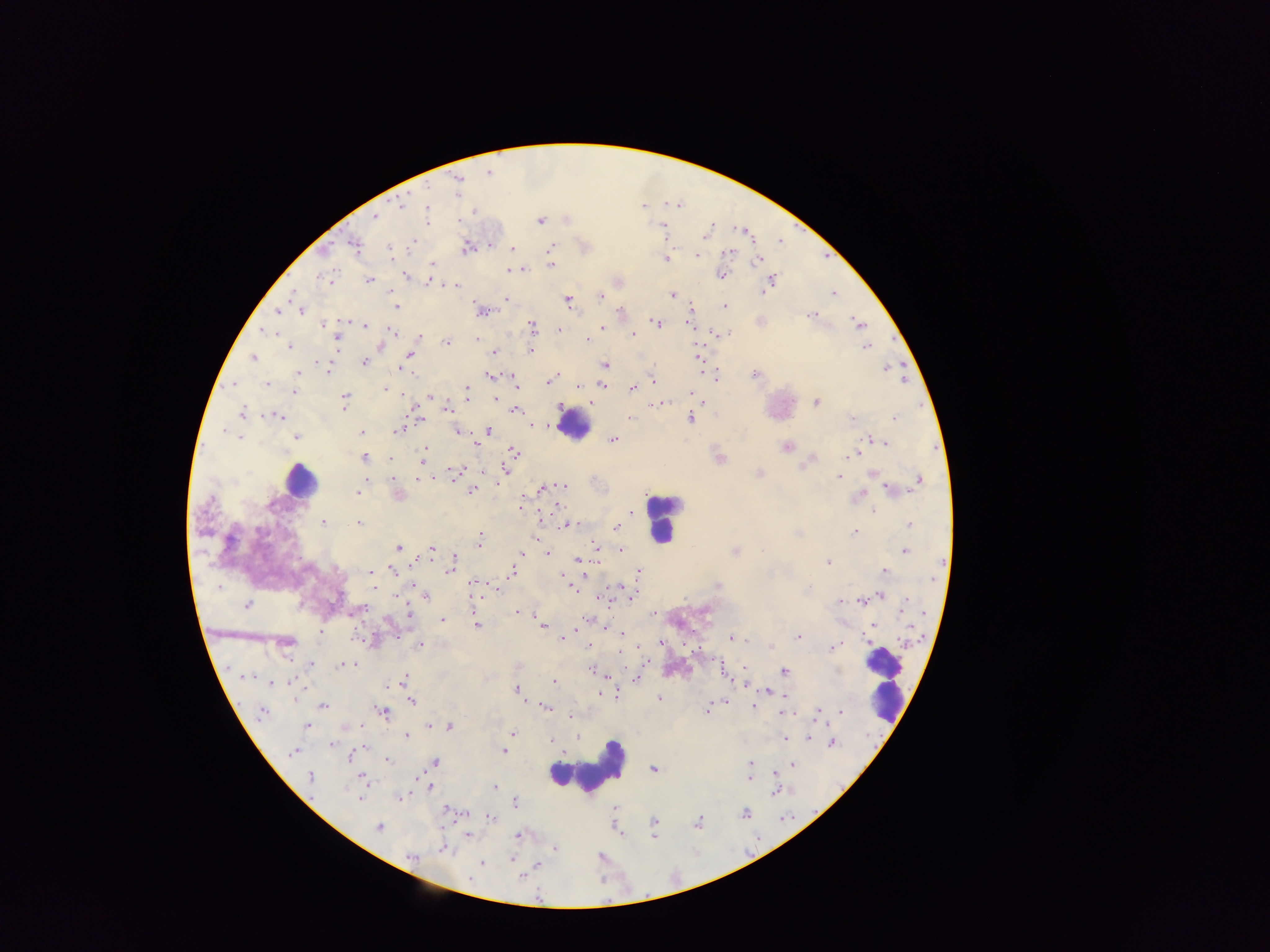
Approximate centers as {x, y} in pixels. Plasmodium parasite locations: {489, 173}, {457, 186}, {402, 205}, {642, 206}, {428, 210}, {375, 215}, {539, 221}, {663, 227}, {742, 230}, {706, 231}, {413, 242}, {355, 246}, {551, 246}, {466, 247}, {389, 249}, {512, 249}, {728, 252}, {697, 255}, {666, 259}, {757, 260}, {432, 264}, {551, 265}, {509, 270}, {516, 270}, {720, 274}, {405, 275}, {327, 277}, {369, 280}, {771, 282}, {454, 285}, {833, 293}, {600, 295}, {672, 295}, {505, 300}, {568, 302}, {396, 306}, {725, 307}, {692, 309}, {277, 310}, {481, 310}, {301, 311}, {621, 311}, {810, 316}, {690, 320}, {656, 323}, {859, 324}, {326, 325}, {365, 325}, {532, 326}, {603, 328}, {559, 330}, {264, 332}, {392, 332}, {633, 334}, {723, 334}, {420, 336}, {337, 338}, {476, 338}, {588, 339}, {446, 342}, {289, 347}, {865, 347}, {532, 350}, {495, 352}, {410, 355}, {253, 358}, {698, 358}, {364, 363}, {604, 365}, {323, 366}, {401, 367}, {885, 368}, {298, 372}, {755, 374}, {490, 376}, {554, 376}, {717, 377}, {652, 380}, {549, 381}, {233, 384}, {266, 385}, {603, 385}, {578, 386}, {385, 389}, {632, 389}, {466, 390}, {295, 391}, {692, 394}, {694, 396}, {431, 397}, {495, 398}, {345, 401}, {816, 402}, {661, 404}, {655, 405}, {447, 409}, {517, 410}, {242, 412}, {277, 416}, {630, 418}, {690, 418}, {894, 418}, {851, 419}, {533, 427}, {399, 429}, {457, 430}, {488, 431}, {362, 433}, {296, 436}, {239, 437}, {613, 439}, {873, 439}, {882, 442}, {476, 443}, {786, 446}, {514, 452}, {422, 454}, {853, 455}, {364, 458}, {719, 458}, {506, 469}, {456, 472}, {760, 474}, {839, 476}, {392, 478}, {424, 479}, {919, 479}, {563, 486}, {542, 488}, {892, 490}, {471, 491}, {358, 492}, {398, 495}, {857, 495}, {521, 506}, {874, 510}, {632, 513}, {323, 523}, {358, 523}, {570, 524}, {909, 525}, {616, 526}, {855, 531}, {479, 539}, {534, 539}, {399, 548}, {433, 548}, {597, 548}, {621, 550}, {904, 551}, {734, 552}, {521, 554}, {547, 554}, {454, 559}, {578, 559}, {827, 562}, {450, 568}, {393, 570}, {639, 571}, {512, 572}, {884, 572}, {371, 573}, {564, 579}, {475, 585}, {373, 586}, {718, 586}, {219, 587}, {575, 589}, {633, 594}, {426, 595}, {880, 595}, {840, 602}, {862, 602}, {246, 605}, {904, 608}, {517, 612}, {409, 614}, {654, 614}, {443, 620}, {476, 625}, {542, 625}, {620, 633}, {798, 636}, {562, 638}, {731, 638}, {661, 643}, {287, 644}, {420, 645}, {588, 645}, {834, 647}, {772, 648}, {312, 664}, {344, 665}, {744, 668}, {593, 670}, {783, 672}, {728, 674}, {247, 677}, {636, 679}, {403, 680}, {273, 683}, {553, 683}, {395, 684}, {518, 691}, {768, 692}, {601, 695}, {659, 698}, {411, 700}, {323, 705}, {753, 705}, {546, 707}, {707, 709}, {263, 711}, {383, 712}, {840, 712}, {784, 713}, {818, 713}, {572, 717}, {307, 727}, {448, 727}, {512, 733}, {406, 736}, {785, 738}, {806, 738}, {550, 741}, {331, 744}, {831, 744}, {292, 751}, {361, 751}, {504, 751}, {352, 758}, {388, 760}, {750, 763}, {435, 764}, {792, 765}, {653, 769}, {311, 777}, {749, 778}, {364, 780}, {494, 787}, {430, 788}, {774, 791}, {400, 797}, {360, 798}, {516, 802}, {744, 814}, {491, 818}, {655, 823}, {697, 824}, {378, 827}, {653, 831}, {468, 835}, {518, 836}, {554, 848}, {442, 849}, {411, 857}, {480, 864}, {538, 864}, {523, 876}. Leukocyte locations: {575, 425}, {299, 480}, {661, 519}, {885, 684}, {587, 767}. One field of view. Sample from Ghana. Photographed through a microscope with a mobile-phone camera. Image is 1270×952 pixels. Thick blood film.